Report the malaria status of this cell.
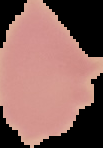

Uninfected.

From a thin blood film. Image is 103×148 pixels. Cell region segmented out of the field of view; the surrounding area is masked to black.